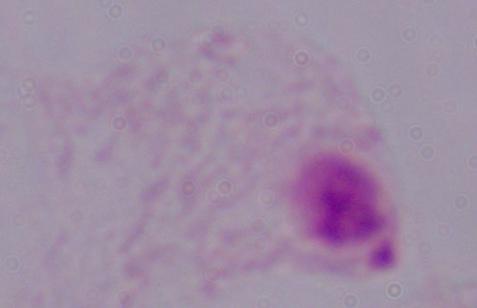
Captured at 1000x magnification. Micrograph. A trichomonad is seen.